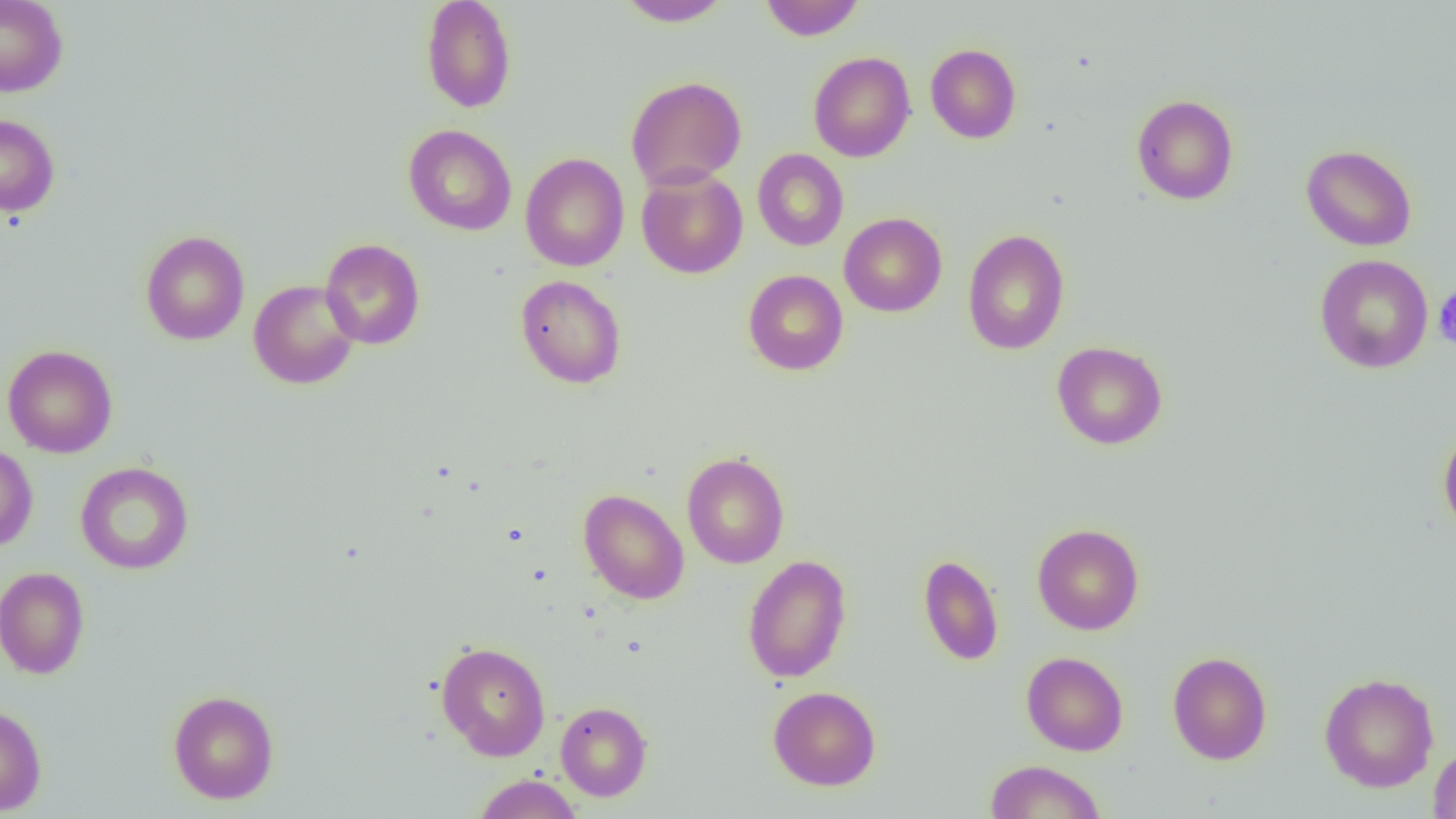
slide-level diagnosis = no evidence of blood parasites
image size = 1456×819 pixels
uninfected red blood cell locations = approximate bounding boxes as named x1/y1/x2/y2 corners in pixels: (x1=0, y1=0, x2=68, y2=97), (x1=421, y1=0, x2=516, y2=113), (x1=616, y1=0, x2=732, y2=27), (x1=759, y1=0, x2=865, y2=41), (x1=925, y1=43, x2=1021, y2=143), (x1=808, y1=51, x2=915, y2=162), (x1=626, y1=76, x2=747, y2=191), (x1=1132, y1=95, x2=1239, y2=205), (x1=0, y1=113, x2=60, y2=216), (x1=403, y1=124, x2=517, y2=236), (x1=1301, y1=144, x2=1417, y2=251), (x1=753, y1=148, x2=849, y2=251), (x1=520, y1=153, x2=630, y2=272), (x1=636, y1=167, x2=748, y2=279), (x1=838, y1=212, x2=947, y2=317), (x1=962, y1=228, x2=1070, y2=355), (x1=140, y1=230, x2=249, y2=345), (x1=320, y1=238, x2=425, y2=350), (x1=1314, y1=254, x2=1433, y2=373), (x1=743, y1=270, x2=848, y2=375), (x1=515, y1=274, x2=626, y2=389), (x1=248, y1=279, x2=360, y2=389), (x1=1051, y1=341, x2=1168, y2=450), (x1=2, y1=344, x2=118, y2=458), (x1=1438, y1=427, x2=1456, y2=538), (x1=0, y1=445, x2=38, y2=553), (x1=682, y1=452, x2=790, y2=569), (x1=75, y1=461, x2=194, y2=574), (x1=578, y1=488, x2=690, y2=604), (x1=1032, y1=523, x2=1144, y2=635), (x1=919, y1=553, x2=1004, y2=666), (x1=742, y1=554, x2=852, y2=683), (x1=0, y1=566, x2=90, y2=679), (x1=436, y1=641, x2=551, y2=760), (x1=1021, y1=651, x2=1128, y2=756), (x1=1167, y1=651, x2=1272, y2=764), (x1=1318, y1=672, x2=1439, y2=792), (x1=768, y1=686, x2=881, y2=790), (x1=168, y1=689, x2=279, y2=804), (x1=555, y1=701, x2=653, y2=801), (x1=0, y1=704, x2=47, y2=815), (x1=1428, y1=743, x2=1456, y2=819), (x1=984, y1=759, x2=1106, y2=818), (x1=472, y1=774, x2=583, y2=818)
preparation = thin blood smear
platelet locations = approximate bounding boxes as named x1/y1/x2/y2 corners in pixels: (x1=1433, y1=288, x2=1456, y2=349)
magnification = 1000x
modality = optical microscopy
field of view = single